Report the malaria status of this cell.
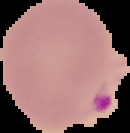
Parasitized.

From a thin blood film. Segmented cell region on a black background. Image is 130×133 pixels.